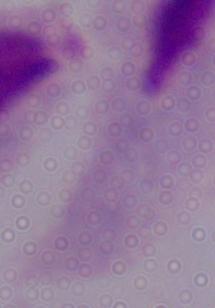
modality = photomicrograph
identification = trichomonad
magnification = 1000x